State the blood parasite species.
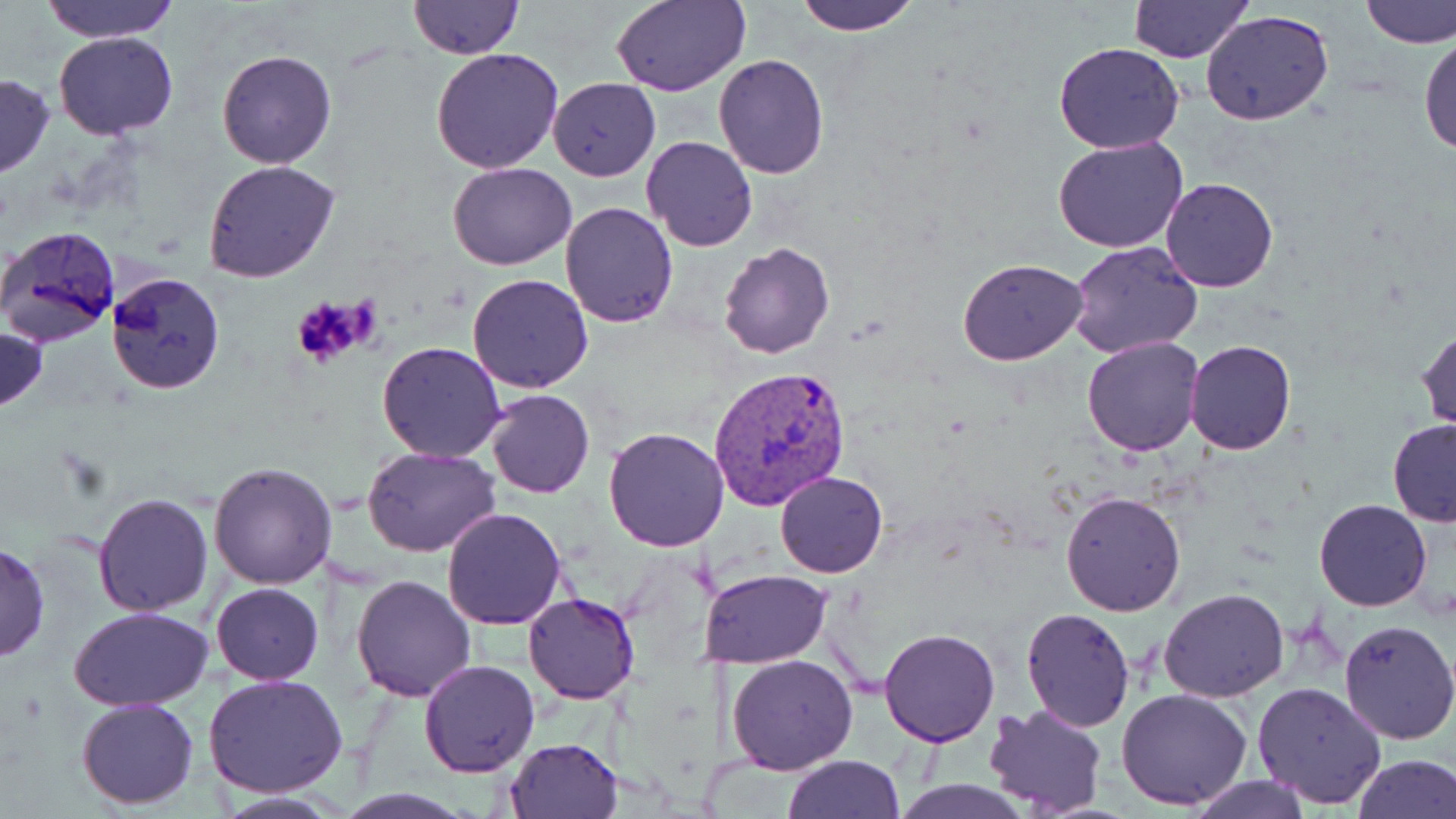
Plasmodium vivax.

Summary:
  - Coordinate format: approximate bounding boxes as (x1, y1, x2, y2) in pixels
  - Plasmodium vivax-infected red blood cell locations: (708, 365, 852, 509)
  - Uninfected red blood cell locations: (39, 0, 182, 43), (611, 0, 750, 96), (792, 0, 924, 35), (1356, 0, 1455, 49), (408, 1, 524, 61), (1129, 1, 1253, 64), (1201, 10, 1334, 127), (1419, 31, 1456, 155), (55, 32, 179, 139), (1053, 40, 1186, 153), (430, 47, 566, 173), (217, 49, 338, 169), (713, 54, 830, 177), (0, 73, 53, 177), (548, 78, 660, 181), (641, 136, 758, 254), (1053, 137, 1188, 254), (204, 161, 340, 283), (449, 161, 577, 271), (1159, 177, 1281, 293), (561, 201, 677, 326), (3, 225, 123, 348), (1068, 239, 1204, 359), (717, 241, 835, 360), (957, 257, 1089, 366), (107, 271, 226, 394), (467, 273, 593, 393), (0, 325, 48, 413), (1416, 327, 1455, 434), (1081, 336, 1206, 456), (1185, 340, 1297, 455), (377, 341, 508, 462), (486, 389, 594, 498), (1386, 418, 1456, 527), (603, 426, 730, 552), (361, 447, 501, 558), (209, 460, 338, 590), (775, 471, 888, 578), (1059, 491, 1186, 614), (93, 493, 214, 616), (1313, 499, 1432, 611), (442, 506, 568, 629), (0, 541, 49, 664), (699, 569, 831, 669), (350, 574, 475, 702), (211, 583, 323, 684), (1159, 587, 1289, 703), (524, 591, 640, 705), (69, 606, 212, 712), (1020, 607, 1137, 731), (1339, 618, 1456, 746), (879, 628, 1001, 746), (726, 652, 858, 774), (419, 660, 540, 777), (203, 674, 348, 798), (1252, 681, 1387, 809), (1118, 688, 1252, 809), (76, 696, 200, 808), (983, 704, 1110, 818), (505, 737, 622, 819), (783, 753, 906, 819), (1351, 753, 1456, 819), (1187, 774, 1313, 818), (891, 779, 1032, 818), (209, 792, 345, 819)
  - Platelet locations: (290, 296, 369, 369)
  - Magnification: 1000x
  - Stain: May-Grünwald-Giemsa
  - Image size: 1456×819 pixels
  - Field of view: single
  - Modality: light microscopy
  - Preparation: thin blood smear